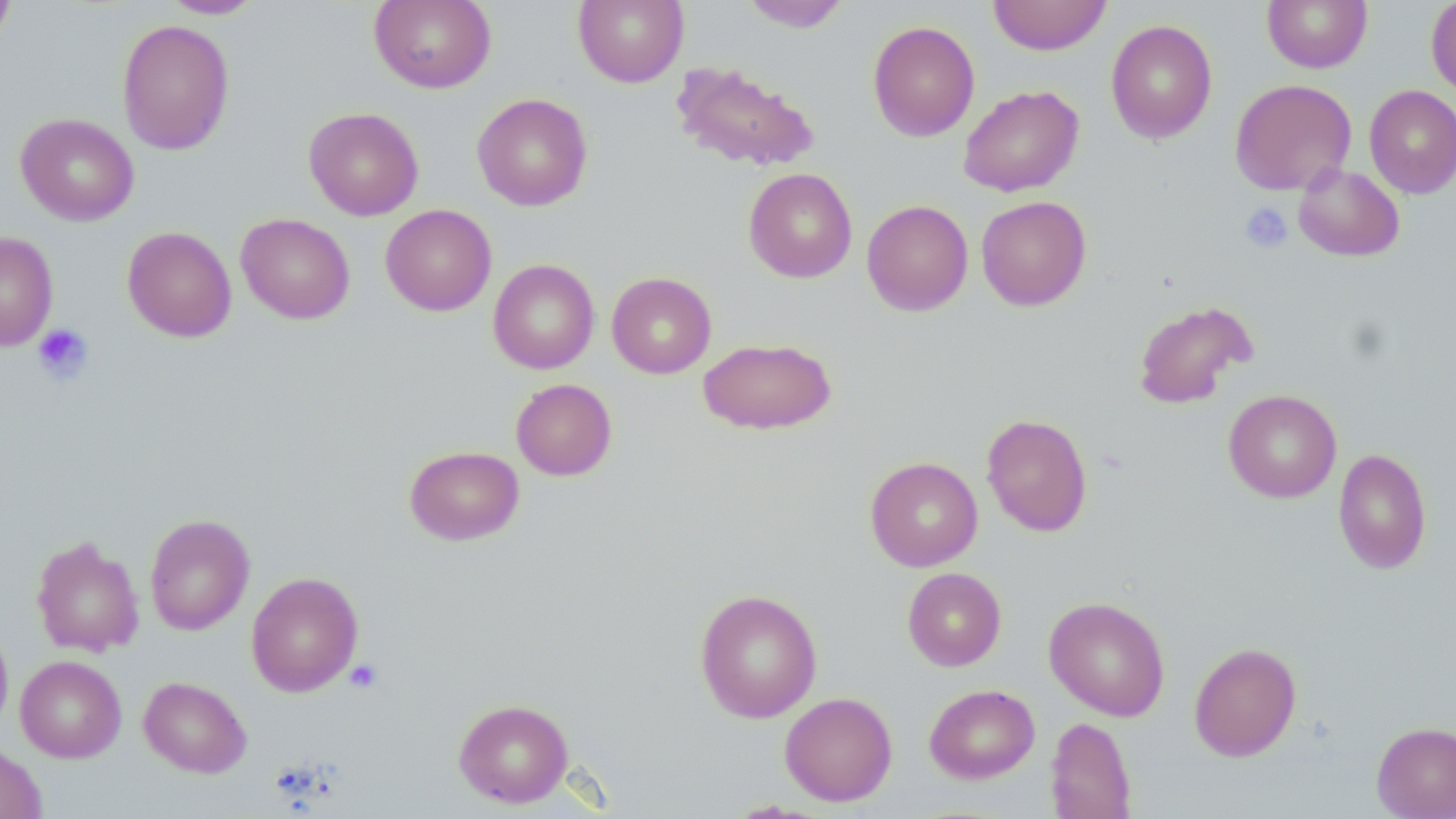
slide-level diagnosis = negative for blood parasites
field of view = single
modality = optical microscopy
magnification = 1000x
stain = May-Grünwald-Giemsa
preparation = thin blood smear
image size = 1456×819 pixels
platelet locations = approximate bounding boxes as [x1, y1, x2, y2] in pixels: [1239, 202, 1293, 253], [32, 323, 94, 384], [345, 659, 383, 693]
uninfected red blood cell locations = approximate bounding boxes as [x1, y1, x2, y2] in pixels: [0, 0, 16, 47], [161, 0, 263, 19], [369, 0, 496, 93], [573, 0, 689, 87], [739, 0, 851, 32], [989, 0, 1111, 55], [1262, 0, 1372, 73], [1426, 0, 1456, 98], [116, 18, 235, 155], [1105, 19, 1218, 144], [867, 20, 980, 142], [671, 61, 820, 173], [1229, 79, 1357, 195], [958, 85, 1084, 197], [1364, 85, 1456, 198], [472, 93, 593, 211], [303, 106, 424, 220], [15, 112, 139, 226], [1293, 164, 1405, 262], [743, 167, 857, 283], [976, 196, 1091, 310], [861, 199, 974, 316], [380, 204, 497, 316], [236, 213, 355, 324], [122, 226, 236, 343], [0, 231, 59, 351], [488, 259, 600, 374], [607, 272, 717, 378], [1132, 299, 1258, 409], [697, 336, 836, 435], [510, 378, 617, 480], [1223, 389, 1342, 502], [981, 413, 1093, 536], [404, 445, 525, 545], [1333, 447, 1431, 575], [865, 456, 983, 572], [144, 514, 255, 635], [31, 535, 144, 656], [902, 567, 1006, 671], [246, 571, 363, 697], [695, 588, 822, 723], [1044, 596, 1170, 721], [0, 615, 13, 735], [1188, 641, 1302, 761], [15, 655, 126, 762], [138, 675, 252, 778], [924, 684, 1040, 783], [779, 691, 898, 806], [453, 698, 573, 807], [1045, 716, 1136, 818], [1372, 720, 1456, 819], [0, 743, 47, 819]